Comment on the morphology of the erythrocytes.
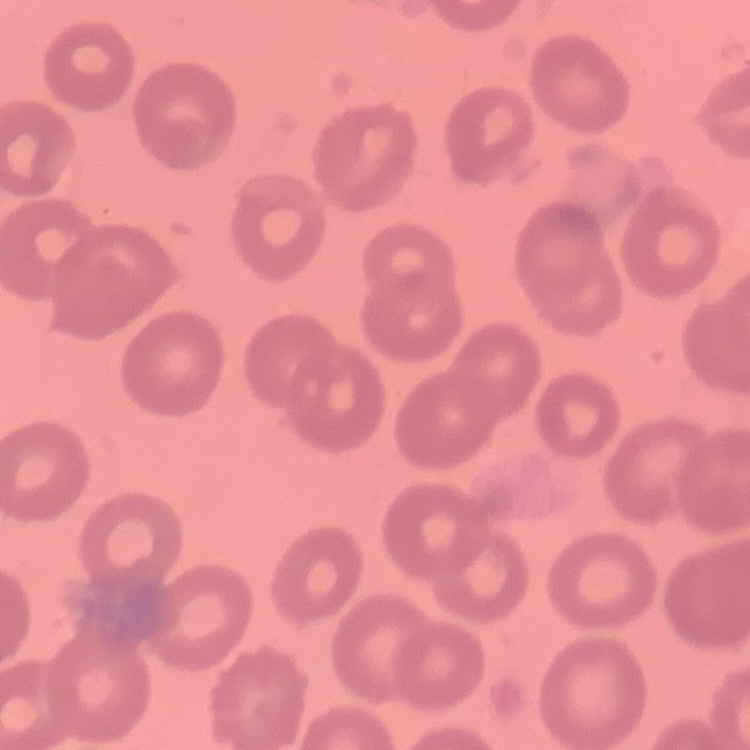
No rouleaux formation.

Square crop of a larger photomicrograph. Stained with either Field's or Giemsa. Thin blood film.